Point out each leukocyte.
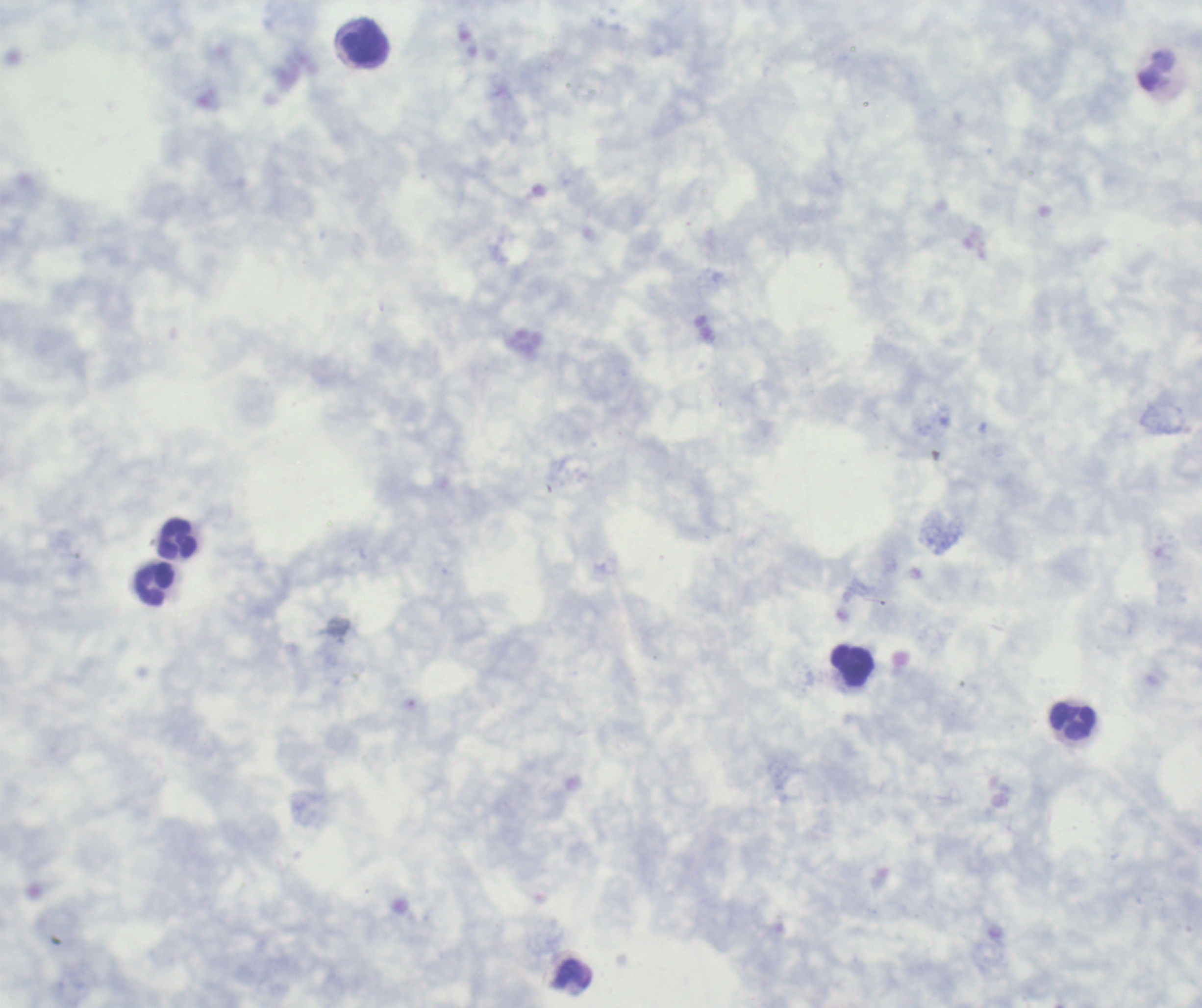
Approximate centers as {x, y} in pixels.
Leukocytes: {366, 45}, {178, 539}, {156, 585}, {853, 666}, {1073, 721}, {574, 975}.

Thick smear of blood. Result: negative for malaria parasites. Romanowsky-stained preparation. Coloration quality: good. Background quality: poor. Captured at 100x magnification. Image is 1202×1008 pixels. Single field of view. Previously used in an actual diagnosis.